Assess this cell for malaria.
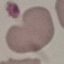
It is uninfected.

capture: smartphone through the microscope eyepiece
stain: Giemsa
preparation: thin blood film
image_type: automatically extracted cell patch, resized to 64 × 64 pixels